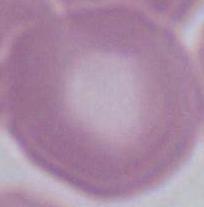

modality = micrograph
identification = erythrocyte
magnification = 1000x